State which parasite is depicted.
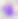
Toxoplasma gondii.

magnification = 400x
modality = photomicrograph